Report the malaria status of this cell.
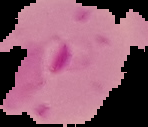

Parasitized.

From a thin blood film. Segmented cell region on a black background. Image is 148×127 pixels.